Classify this cell by malaria status.
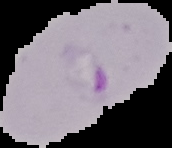
Parasitized.

Segmented cell region on a black background. Image is 172×148 pixels. From a thin blood film.